Give the preparation type.
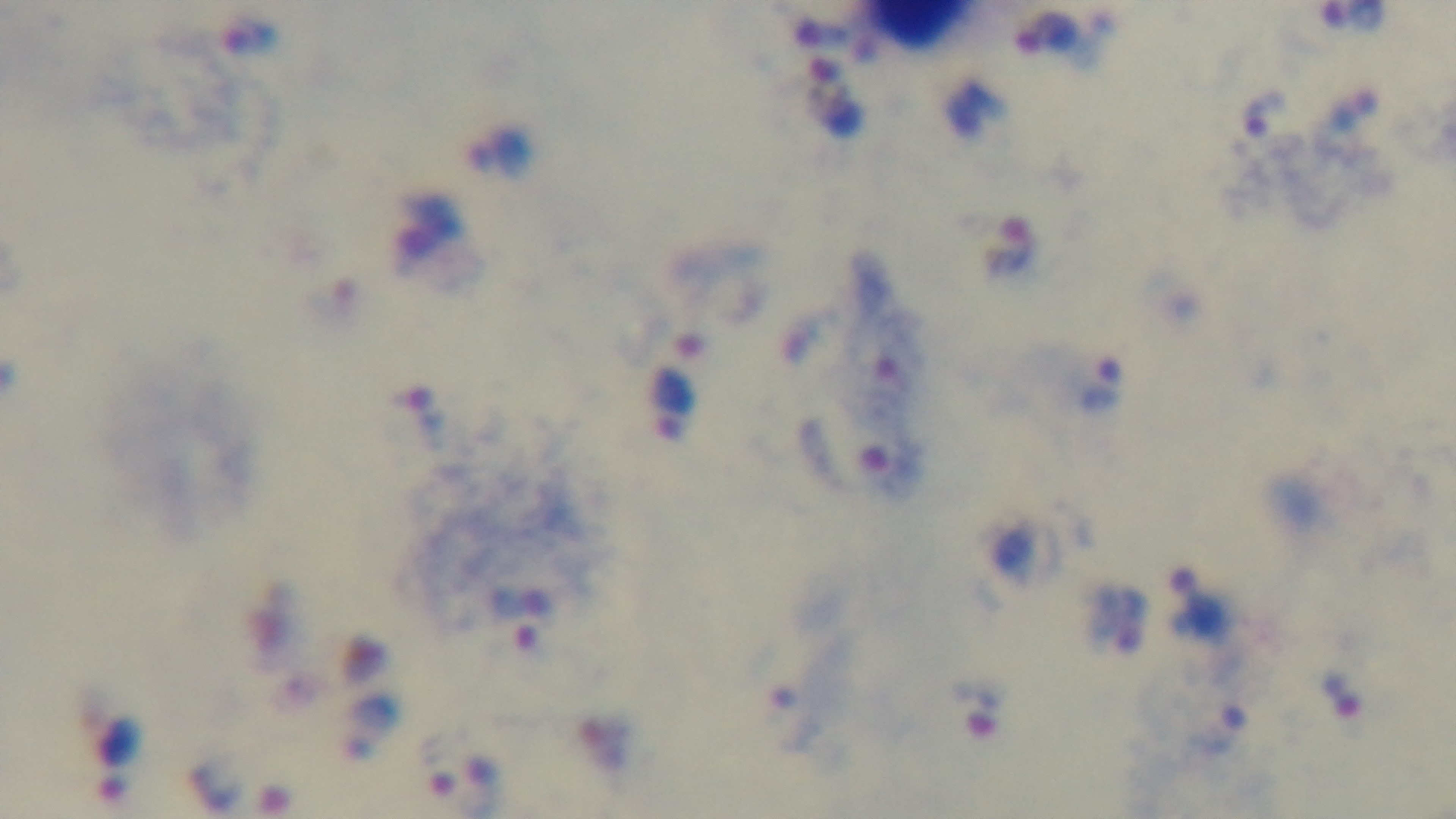
It is a thick blood film.

Summary:
  - Field of view: one from the slide
  - Objective: 100x oil immersion
  - Modality: light microscopy
  - Stain: Giemsa
  - Malaria status: positive
  - Capture: mounted 4K digital camera